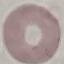

{
  "result": "negative for malaria parasites",
  "capture": "smartphone camera at the microscope eyepiece",
  "image_type": "automatically extracted cell patch, resized to 64 × 64 pixels",
  "stain": "Giemsa",
  "preparation": "thin smear"
}